State which parasite is depicted.
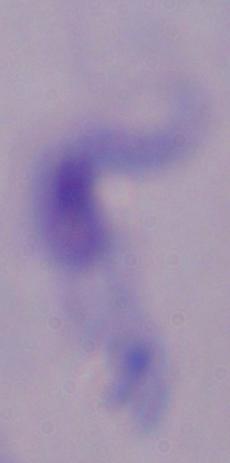

This is a trypanosome.

Summary:
  - Magnification: 1000x
  - Modality: micrograph